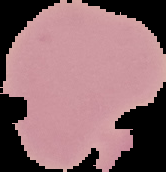 Result: negative for Plasmodium parasites. From a thin blood smear. Segmented cell region on a black background. Image is 166×172 pixels.